Identify the blood parasite species.
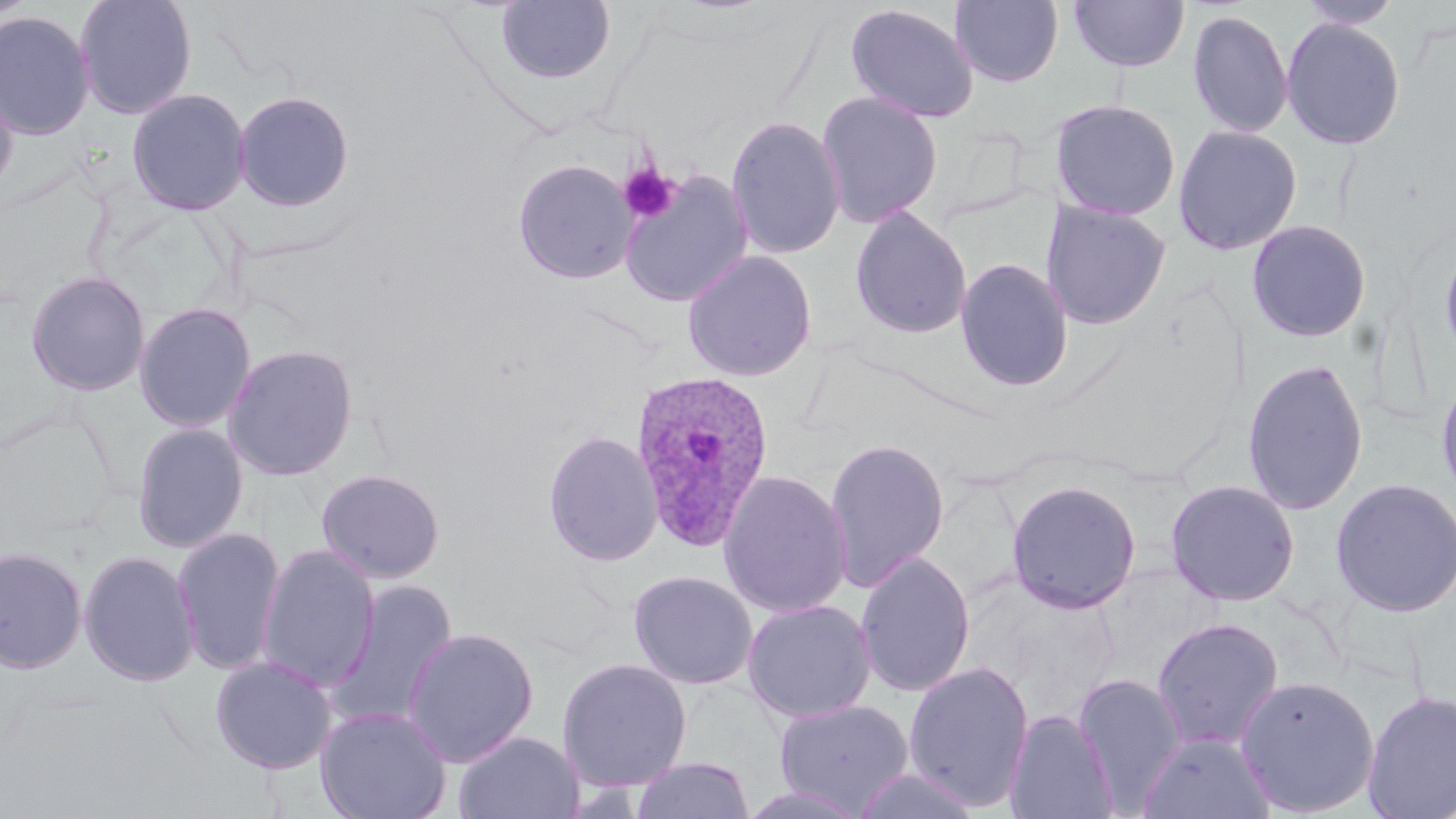

Plasmodium ovale.

Summary:
  - Coordinate format: approximate bounding boxes as [x1, y1, x2, y2] in pixels
  - Uninfected red blood cell locations: [73, 0, 197, 119], [1296, 0, 1404, 30], [495, 1, 616, 85], [949, 1, 1064, 88], [1068, 1, 1190, 73], [845, 4, 979, 124], [1186, 9, 1294, 139], [0, 10, 96, 140], [1281, 17, 1406, 150], [0, 79, 18, 199], [127, 87, 251, 216], [233, 90, 355, 212], [816, 92, 943, 227], [1050, 99, 1181, 221], [726, 115, 846, 260], [1172, 124, 1302, 256], [513, 159, 637, 285], [618, 171, 754, 308], [1040, 201, 1171, 330], [849, 206, 972, 340], [1246, 219, 1372, 342], [1437, 234, 1456, 372], [681, 250, 816, 381], [955, 258, 1074, 392], [25, 270, 151, 396], [134, 302, 256, 433], [222, 344, 359, 481], [1242, 358, 1370, 515], [1435, 365, 1456, 507], [131, 422, 248, 553], [543, 429, 664, 567], [823, 438, 949, 592], [316, 468, 445, 583], [718, 469, 852, 618], [1329, 477, 1456, 619], [1006, 479, 1142, 614], [1165, 479, 1301, 607], [172, 526, 286, 675], [256, 544, 380, 692], [0, 545, 88, 674], [79, 549, 200, 687], [855, 552, 976, 697], [628, 570, 758, 689], [323, 579, 460, 733], [742, 600, 876, 724], [1152, 616, 1284, 751], [401, 626, 539, 766], [210, 655, 338, 774], [557, 657, 692, 790], [903, 661, 1035, 812], [1072, 673, 1186, 812], [1235, 673, 1380, 817], [1362, 689, 1456, 818], [773, 699, 915, 815], [315, 705, 452, 819], [1004, 709, 1119, 819], [453, 730, 584, 818], [1139, 730, 1276, 819], [630, 756, 755, 819], [851, 768, 983, 819], [738, 783, 872, 819]
  - Platelet locations: [618, 162, 681, 224]
  - Plasmodium ovale-infected red blood cell locations: [629, 367, 775, 553]
  - Magnification: 1000x
  - Field of view: one of a larger specimen
  - Image size: 1456×819 pixels
  - Modality: optical microscopy
  - Stain: May-Grünwald-Giemsa
  - Preparation: thin blood film